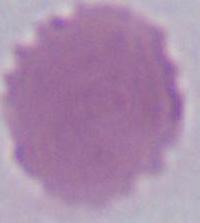 1000x magnification. A red blood cell is shown. Micrograph.